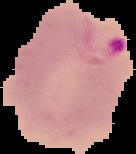
preparation = thin blood smear
malaria status = parasitized
image size = 136×154 pixels
image type = segmented cell region with the area outside set to black